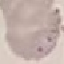

Summary:
  - Result: no malaria parasites detected
  - Capture: smartphone through the microscope eyepiece
  - Preparation: thin blood film
  - Image type: cell patch, automatically extracted from a larger field of view and resized to 64 × 64 pixels
  - Stain: Giemsa